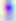
Summary:
  - Identification: Toxoplasma gondii
  - Modality: micrograph
  - Magnification: 400x